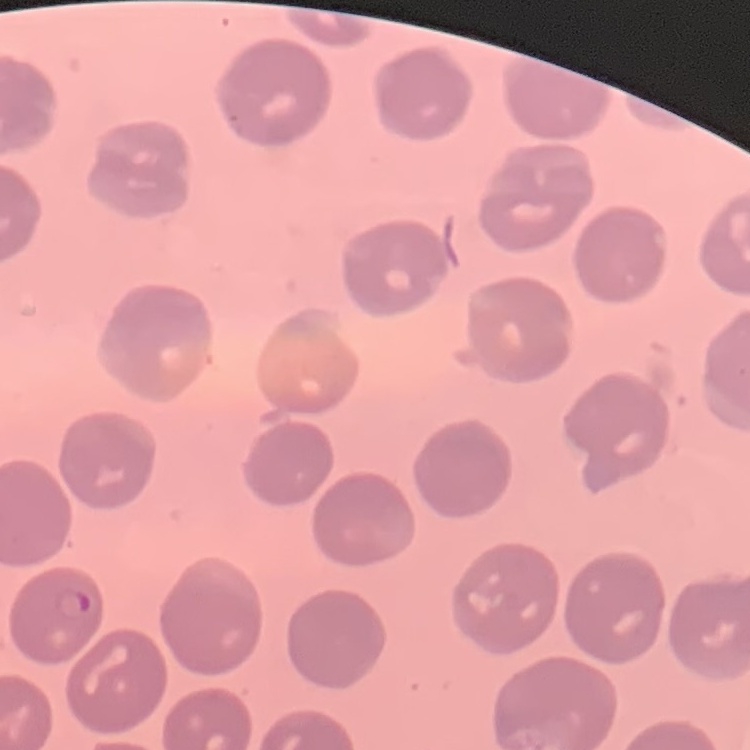
red blood cell morphology = no rouleaux formation
image type = square crop of a larger photomicrograph
stain = Field's or Giemsa
preparation = thin blood film